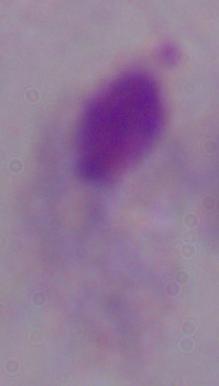 Captured at 1000x magnification. A trichomonad is shown. Photomicrograph.